Identify the preparation type.
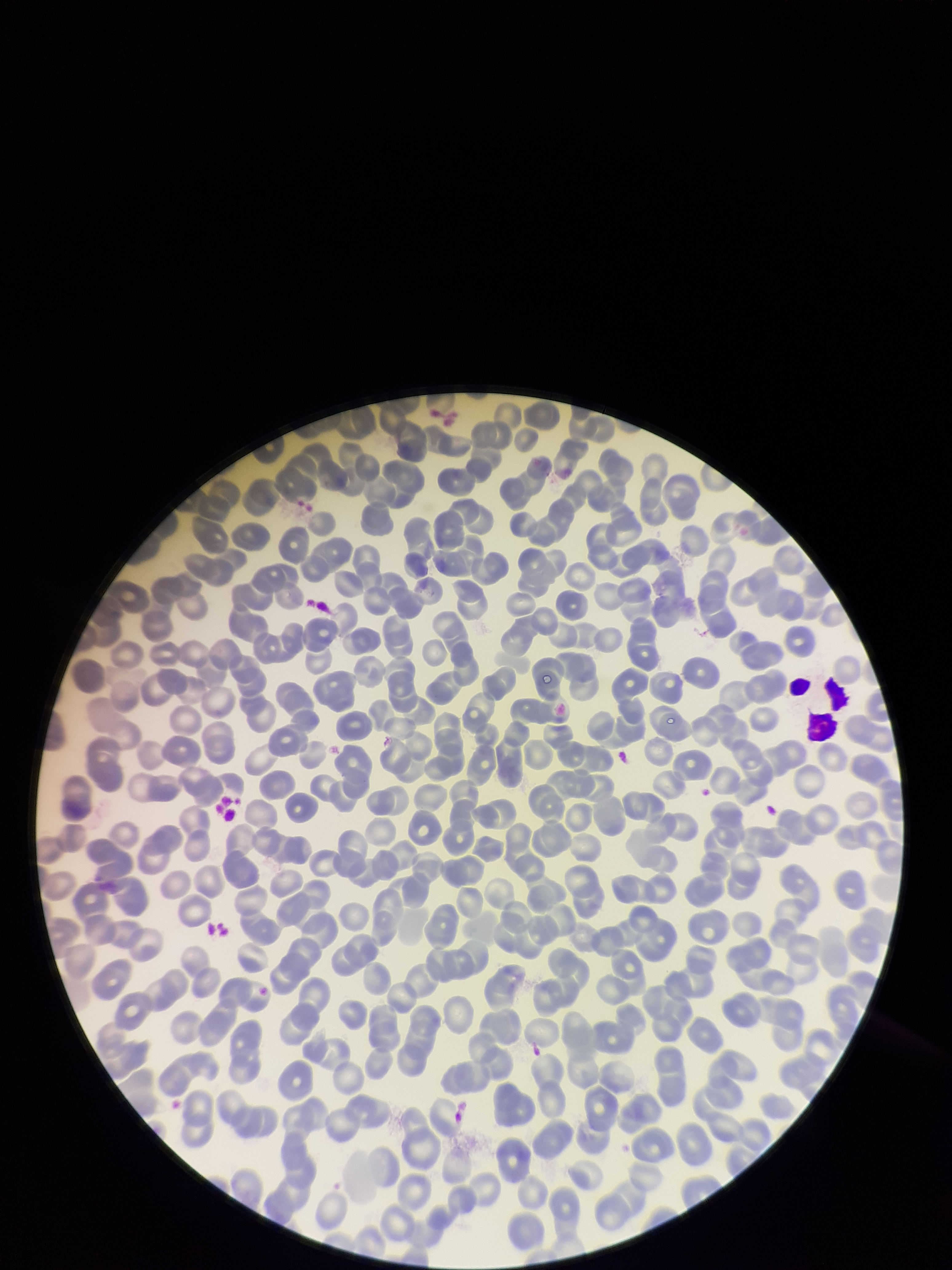

A thin smear.

Summary:
  - Field of view: one from this slide
  - Parasitized red blood cell count: 0
  - Image size: 952×1270 pixels
  - Capture: smartphone photograph through the microscope eyepiece
  - Red blood cell count: 271
  - Stain: Giemsa
  - Patient malaria status: negative
  - Parasitized red blood cells: none identified